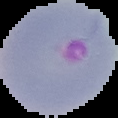 From a thin blood smear. Malaria status: parasitized. Segmented cell region on a black background. Image is 118×118 pixels.